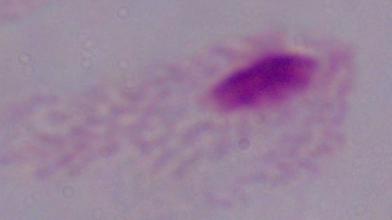
Micrograph. Captured at 1000x magnification. A trichomonad is shown.